Identify the preparation type.
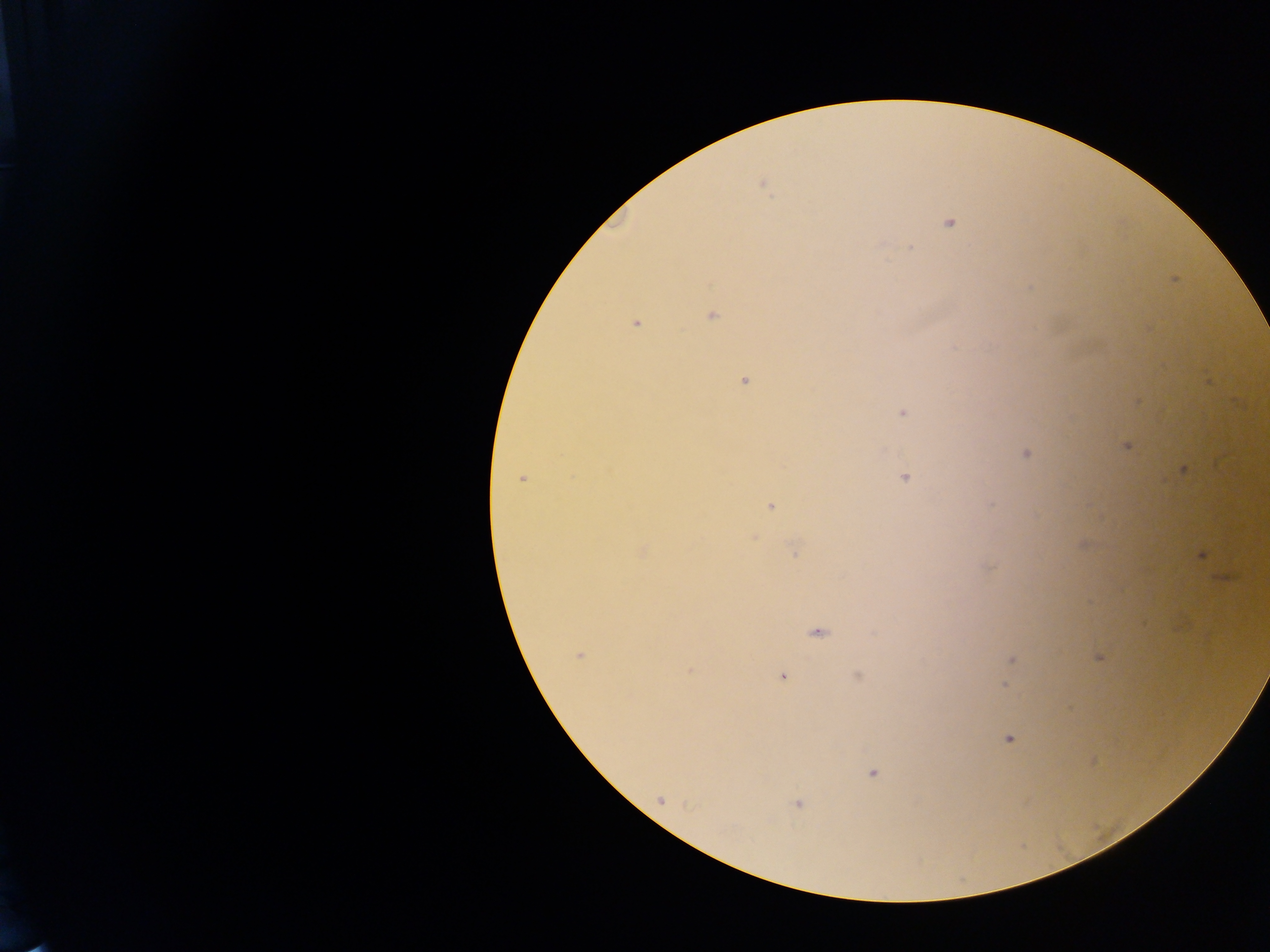
Thick blood smear.

image size = 1270×952 pixels
malaria parasite locations = approximate centers as {x, y} in pixels: {762, 183}, {948, 222}, {909, 248}, {1174, 279}, {710, 314}, {636, 322}, {743, 380}, {1137, 402}, {902, 412}, {1126, 445}, {1026, 453}, {1184, 469}, {904, 477}, {522, 478}, {770, 506}, {753, 536}, {1082, 545}, {641, 550}, {796, 550}, {1200, 555}, {1223, 577}, {816, 631}, {578, 654}, {1099, 657}, {1011, 659}, {689, 670}, {782, 675}, {857, 676}, {1007, 677}, {1004, 685}, {1009, 738}, {1091, 760}, {872, 772}, {660, 800}, {797, 802}
country = Ghana
field of view = single
capture = mobile-phone photograph through a microscope